State which parasite is depicted.
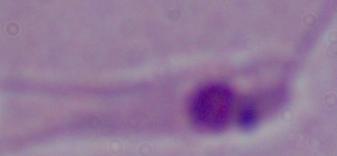
Leishmania.

magnification = 1000x
modality = micrograph